Name the cell type shown.
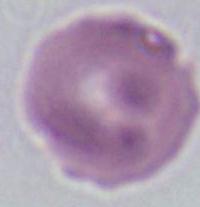
This is an erythrocyte.

Micrograph. Captured at 1000x magnification.